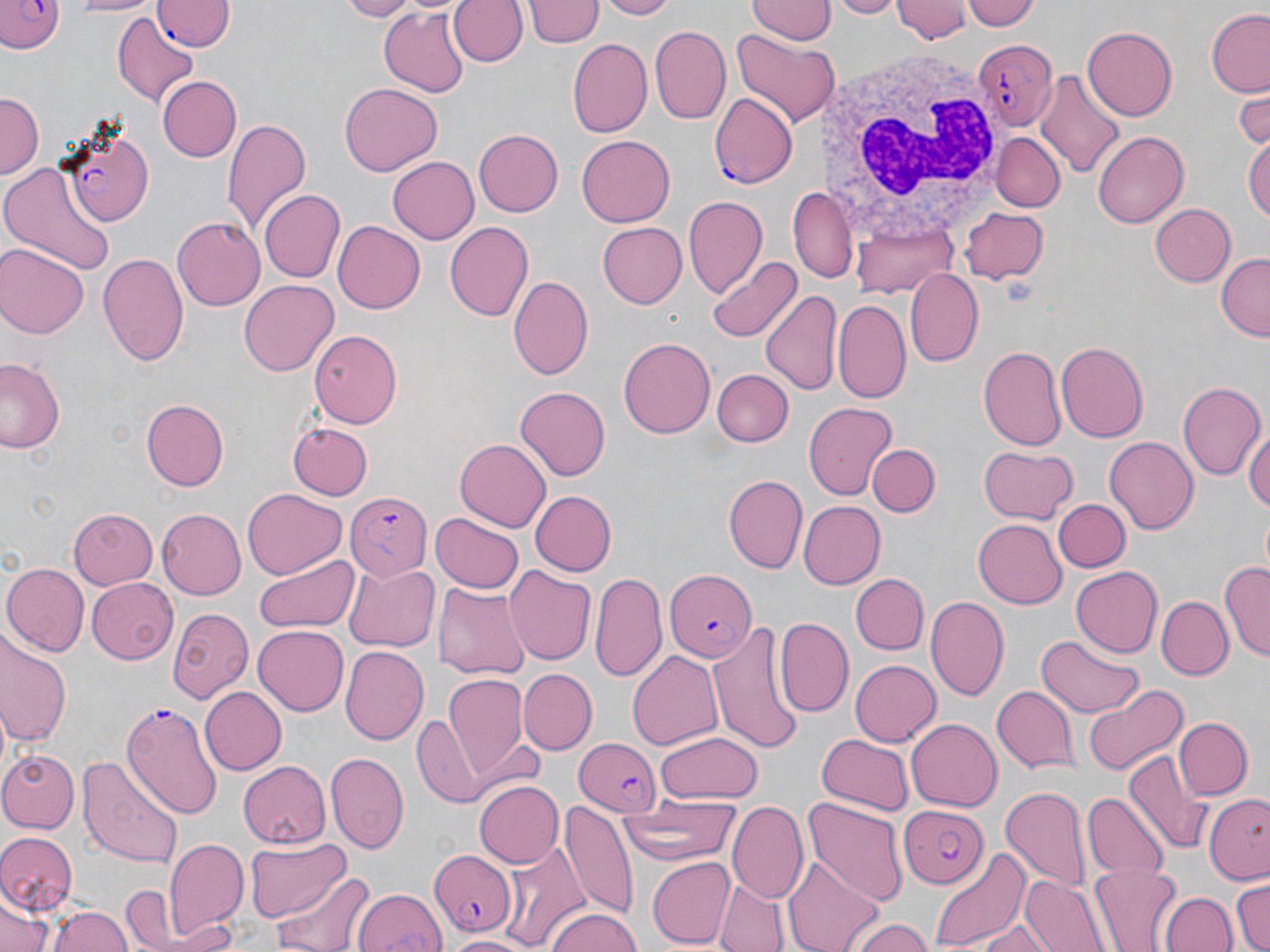
slide-level diagnosis = Plasmodium falciparum
field of view = single
modality = optical microscopy
image size = 1270×952 pixels
uninfected red blood cell locations = approximate bounding boxes as [x1, y1, x2, y2] in pixels: [64, 0, 164, 17], [339, 0, 414, 19], [448, 0, 526, 68], [601, 0, 675, 19], [748, 0, 833, 44], [832, 0, 900, 17], [892, 0, 972, 43], [967, 0, 1041, 32], [525, 1, 603, 49], [378, 5, 470, 96], [741, 7, 836, 85], [1206, 10, 1270, 96], [112, 13, 200, 107], [650, 25, 732, 125], [1083, 26, 1178, 119], [731, 30, 838, 127], [566, 39, 652, 139], [1033, 67, 1127, 180], [156, 75, 241, 162], [339, 82, 441, 175], [163, 86, 285, 193], [1234, 89, 1270, 149], [1, 93, 42, 176], [222, 117, 311, 238], [472, 129, 562, 217], [1091, 129, 1188, 229], [992, 133, 1064, 212], [1245, 134, 1269, 226], [577, 135, 675, 226], [388, 156, 479, 244], [0, 159, 115, 275], [791, 186, 856, 285], [260, 189, 344, 282], [682, 197, 767, 301], [1151, 203, 1235, 287], [960, 206, 1050, 283], [850, 215, 959, 295], [172, 216, 266, 310], [333, 220, 425, 312], [443, 221, 534, 322], [595, 221, 688, 309], [0, 244, 89, 338], [99, 252, 189, 367], [1216, 252, 1269, 341], [709, 256, 802, 343], [904, 267, 984, 366], [508, 273, 593, 382], [239, 280, 339, 377], [760, 290, 842, 400], [834, 299, 910, 403], [310, 329, 401, 428], [619, 335, 718, 438], [1056, 341, 1149, 443], [977, 344, 1068, 451], [2, 358, 62, 454], [711, 369, 793, 447], [1175, 380, 1265, 482], [514, 387, 610, 482], [140, 398, 227, 491], [802, 400, 899, 499], [1245, 421, 1270, 523], [288, 422, 375, 499], [1104, 436, 1198, 537], [455, 439, 550, 529], [868, 443, 938, 517], [979, 446, 1074, 522], [725, 475, 806, 573], [242, 489, 344, 579], [532, 490, 617, 576], [1055, 498, 1128, 573], [800, 500, 884, 589], [71, 509, 158, 591], [155, 509, 245, 599], [432, 513, 524, 594], [973, 519, 1067, 609], [258, 550, 358, 631], [344, 561, 438, 652], [3, 562, 89, 656], [503, 562, 595, 667], [1222, 562, 1270, 661], [1070, 565, 1163, 659], [590, 573, 669, 685], [852, 573, 927, 654], [86, 578, 175, 664], [435, 580, 530, 684], [925, 595, 1009, 699], [1157, 597, 1231, 678], [169, 607, 256, 704], [776, 617, 854, 715], [710, 618, 805, 755], [253, 624, 349, 715], [0, 635, 70, 749], [1038, 635, 1142, 717], [341, 647, 428, 745], [627, 648, 722, 749], [851, 659, 941, 745], [520, 669, 598, 753], [443, 676, 529, 775], [1083, 684, 1188, 778], [200, 687, 287, 775], [991, 687, 1078, 774], [1173, 716, 1254, 798], [412, 717, 487, 806], [907, 718, 1003, 811], [653, 732, 763, 803], [816, 734, 914, 815], [0, 747, 79, 832], [326, 751, 408, 852], [1126, 751, 1210, 857], [76, 754, 183, 869], [239, 761, 334, 848], [471, 780, 561, 870], [1001, 783, 1090, 890], [1083, 792, 1168, 882], [1204, 793, 1270, 883], [799, 795, 909, 906], [561, 801, 638, 922], [727, 802, 809, 905], [612, 807, 743, 867], [0, 831, 77, 914], [165, 837, 248, 939], [504, 839, 593, 950], [246, 840, 347, 922], [927, 845, 1029, 948], [645, 854, 736, 949], [783, 854, 882, 952], [1090, 864, 1179, 950], [277, 869, 375, 952], [120, 870, 218, 952], [1019, 875, 1106, 952], [713, 877, 790, 952], [1232, 877, 1269, 952], [118, 886, 176, 950], [353, 887, 446, 952], [1159, 891, 1237, 952], [0, 894, 52, 952], [46, 905, 130, 952], [543, 909, 645, 952], [846, 914, 935, 952], [170, 917, 244, 952], [968, 921, 1054, 952], [442, 933, 537, 951]
stain = May-Grünwald-Giemsa
magnification = 1000x
preparation = thin blood film
white blood cell locations = approximate bounding boxes as [x1, y1, x2, y2] in pixels: [817, 43, 1015, 249]
Plasmodium falciparum-infected red blood cell locations = approximate bounding boxes as [x1, y1, x2, y2] in pixels: [0, 0, 63, 54], [154, 1, 233, 52], [973, 37, 1058, 130], [709, 91, 799, 190], [59, 124, 156, 225], [344, 492, 431, 581], [663, 568, 755, 662], [120, 701, 222, 819], [573, 737, 664, 818], [899, 804, 989, 887], [426, 849, 513, 936]